Comment on the morphology of the red blood cells.
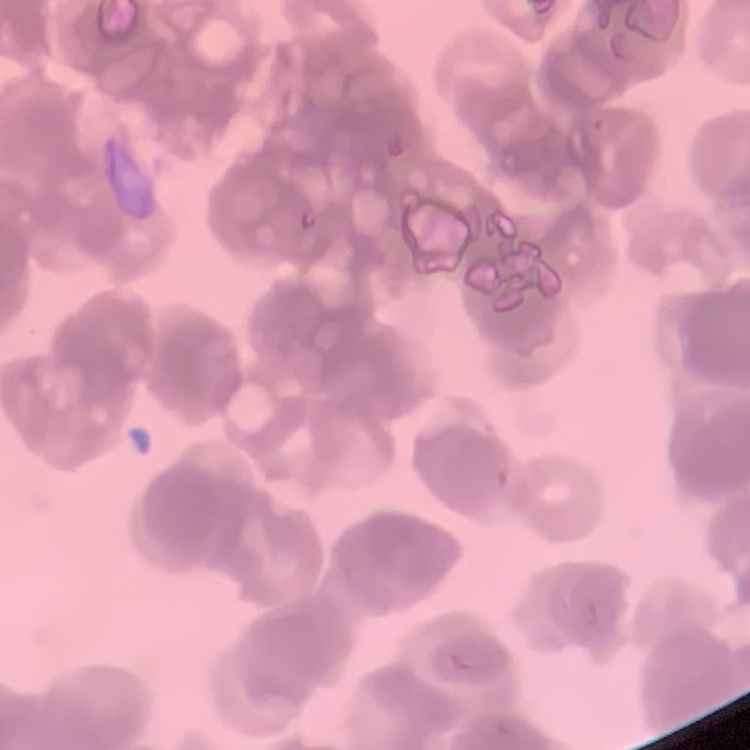
They show rouleaux formation.

stain: Field's or Giemsa
image_type: square crop of a larger photomicrograph
preparation: thin peripheral smear